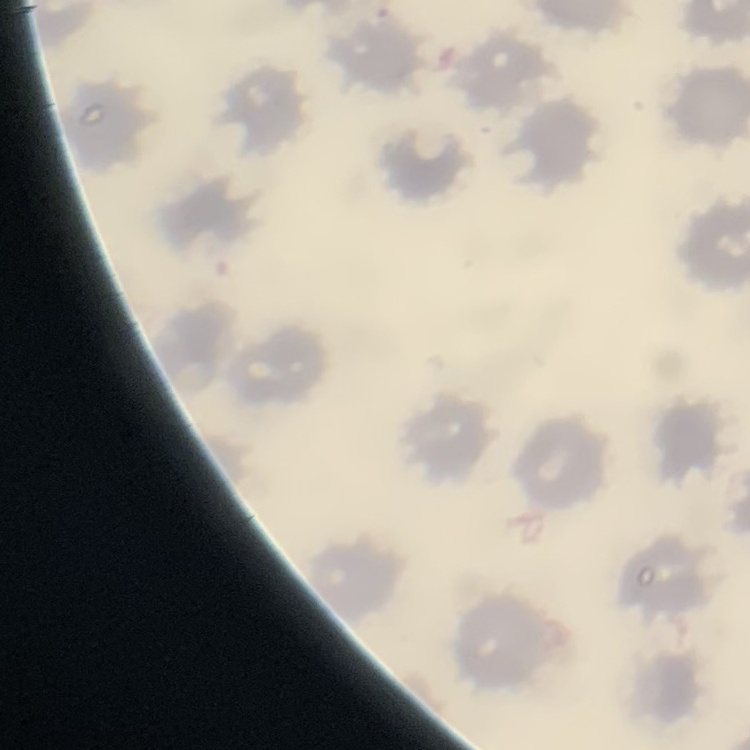

erythrocyte_morphology: no rouleaux formation
stain: Field's or Giemsa
image_type: square crop of a larger photomicrograph
preparation: thin blood smear